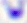
Summary:
  - Modality: photomicrograph
  - Magnification: 400x
  - Identification: Toxoplasma gondii